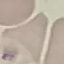 Malaria status: uninfected. Photographed with a smartphone camera at the microscope eyepiece. Giemsa-stained preparation. Thin blood smear. Cell patch, automatically extracted from a larger field of view and resized to 64 × 64 pixels.